Classify this cell by malaria status.
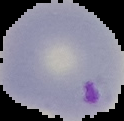

It is parasitized.

From a thin blood smear. Segmented cell region on a black background. Image is 124×121 pixels.